Classify this cell by malaria status.
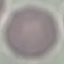
Uninfected.

stain: Giemsa
capture: smartphone camera at the microscope eyepiece
preparation: thin smear
image_type: cell patch, automatically extracted from a larger field of view and resized to 64 × 64 pixels